Find the cells and give the type of each one.
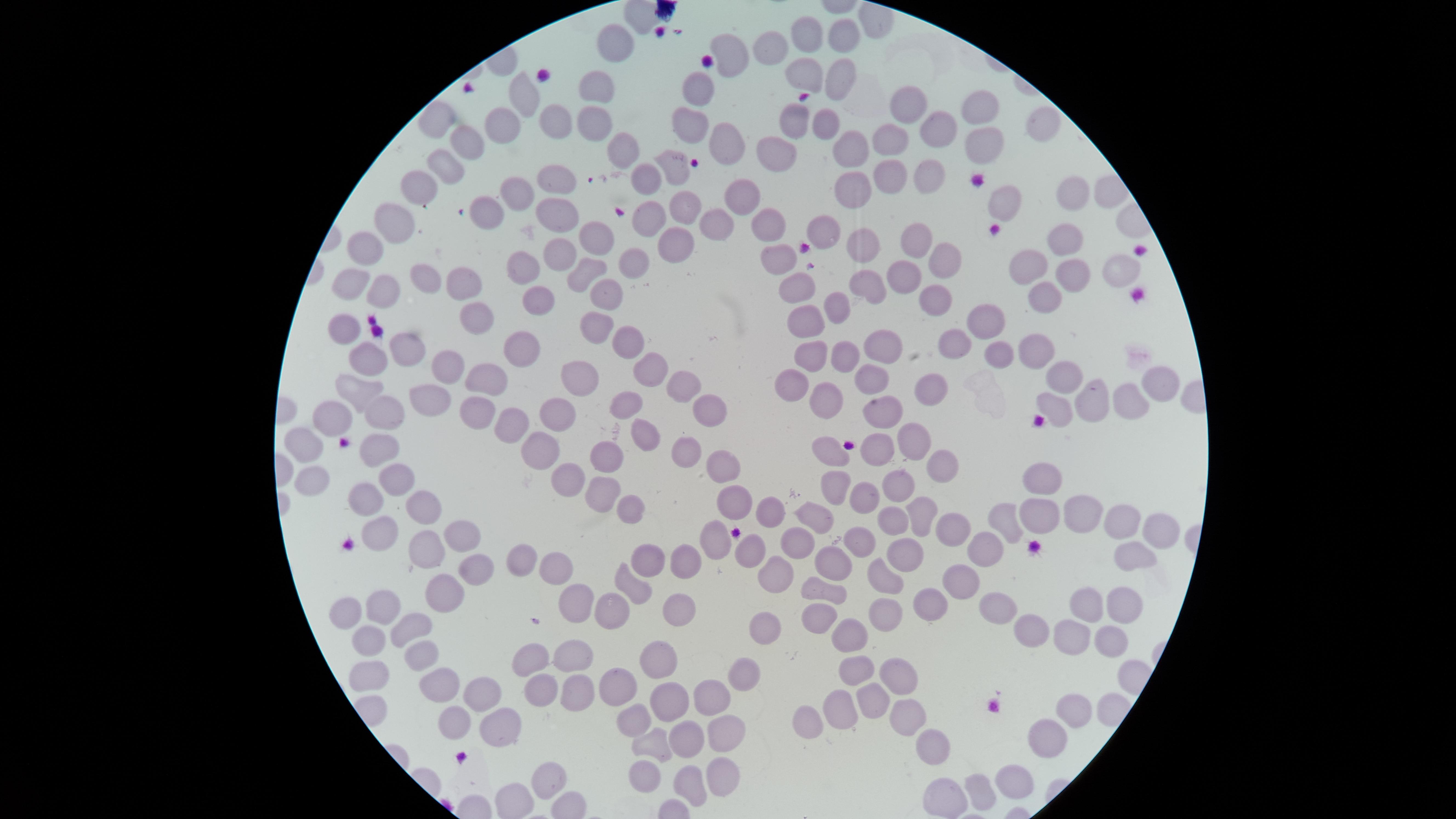

No parasitized red blood cells identified.
Approximate marker points as (x, y) in pixels.
Uninfected red blood cells: (799, 36), (838, 36), (611, 42), (731, 44), (768, 46), (797, 70), (833, 74), (598, 85), (697, 87), (527, 92), (911, 106), (979, 110), (435, 115), (826, 117), (552, 118), (791, 119), (1044, 121), (594, 123), (690, 123), (502, 124), (939, 128), (978, 135), (890, 137), (464, 141), (722, 141), (779, 145), (853, 145), (617, 146), (448, 163), (671, 168), (932, 175), (646, 176), (888, 178), (560, 182), (421, 183), (850, 190), (1072, 191), (515, 193), (737, 193), (1001, 197), (688, 206), (477, 209), (556, 209), (650, 216), (384, 220), (714, 220), (761, 223), (825, 234), (596, 237), (1064, 239), (673, 242), (917, 242), (859, 243), (362, 249), (556, 252), (634, 260), (778, 260), (945, 260), (527, 264), (1036, 264), (1113, 266), (587, 270), (1070, 270), (427, 276), (462, 276), (899, 276), (353, 279), (863, 283), (802, 284), (385, 292), (605, 294), (931, 296), (1041, 296), (539, 299), (835, 307), (474, 311), (988, 313), (347, 320), (801, 320), (598, 322), (886, 338), (959, 339), (625, 340), (406, 343), (523, 345), (1032, 346), (809, 348), (991, 349), (371, 355), (842, 355), (449, 366), (648, 370), (481, 377), (578, 377), (1062, 377), (793, 378), (873, 380), (1159, 382), (680, 384), (923, 388), (822, 393), (358, 394), (427, 399), (1089, 400), (1131, 401), (620, 402), (1053, 403), (882, 404), (708, 406), (378, 407), (554, 408), (478, 413), (334, 416), (511, 425), (913, 435), (636, 438), (538, 440), (300, 444), (381, 445), (877, 448), (686, 449), (835, 449), (606, 458), (940, 464), (723, 468), (391, 478), (567, 479), (1048, 480), (308, 481), (834, 482), (898, 485), (601, 490), (861, 497), (366, 499), (732, 503), (424, 504), (632, 504), (772, 510), (919, 510), (1085, 510), (1035, 513), (890, 514), (1004, 517), (820, 519), (1128, 520), (1160, 529), (377, 530), (460, 531), (950, 531), (715, 538), (801, 539), (861, 541), (429, 545), (984, 547), (746, 553), (910, 554), (831, 558), (1136, 559), (520, 560), (648, 560), (474, 561), (686, 562), (554, 566), (778, 568), (884, 570), (963, 575), (439, 583), (630, 584), (822, 586), (673, 600), (936, 600), (1086, 600), (993, 604), (1123, 604), (386, 605), (609, 606), (349, 608), (576, 609), (886, 611), (825, 612), (762, 626), (413, 628), (1034, 628), (1104, 631), (1067, 632), (850, 634), (369, 638), (658, 655), (424, 659), (529, 659), (572, 659), (855, 665), (898, 667), (374, 673), (738, 674), (439, 681), (621, 681), (482, 687), (539, 688), (580, 690), (705, 695), (869, 698), (670, 700), (1079, 702), (843, 707), (636, 713), (802, 715), (917, 718), (452, 722), (501, 726), (723, 728), (1055, 730), (685, 740), (654, 741), (941, 746), (644, 767), (715, 770), (1011, 775), (550, 779), (689, 784), (981, 793), (945, 795), (511, 797).
No white blood cells identified.

Image is 1456×819 pixels. Thin blood smear. One field of view of the specimen. Giemsa-stained preparation. The visible region is circular. Photographed with a smartphone camera through the microscope eyepiece.